Report the malaria status.
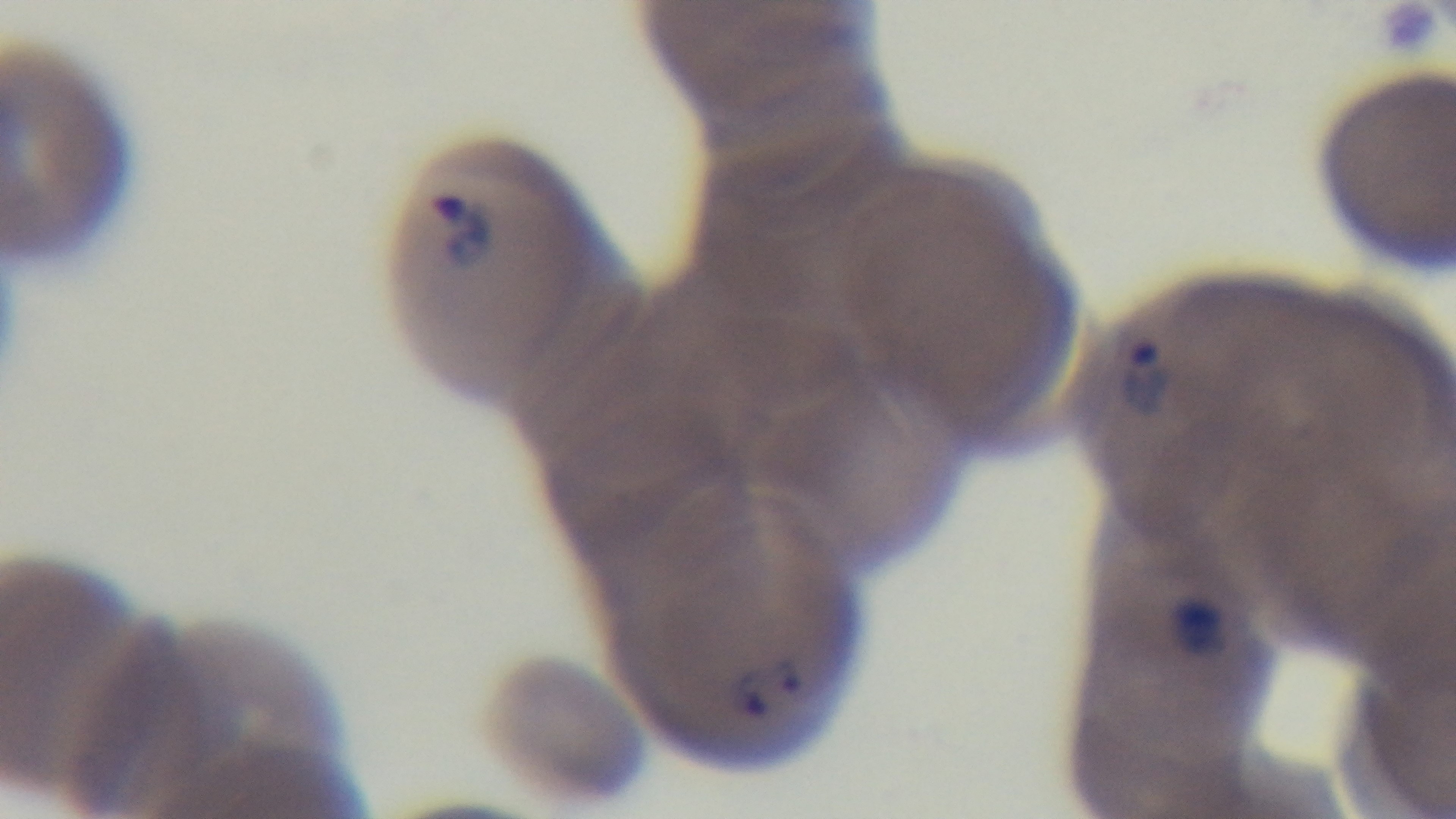
Positive.

Summary:
  - Stain: Giemsa
  - Objective: 100x oil immersion
  - Preparation: thin blood film
  - Field of view: one from the slide
  - Capture: mounted 4K digital camera
  - Modality: light microscopy